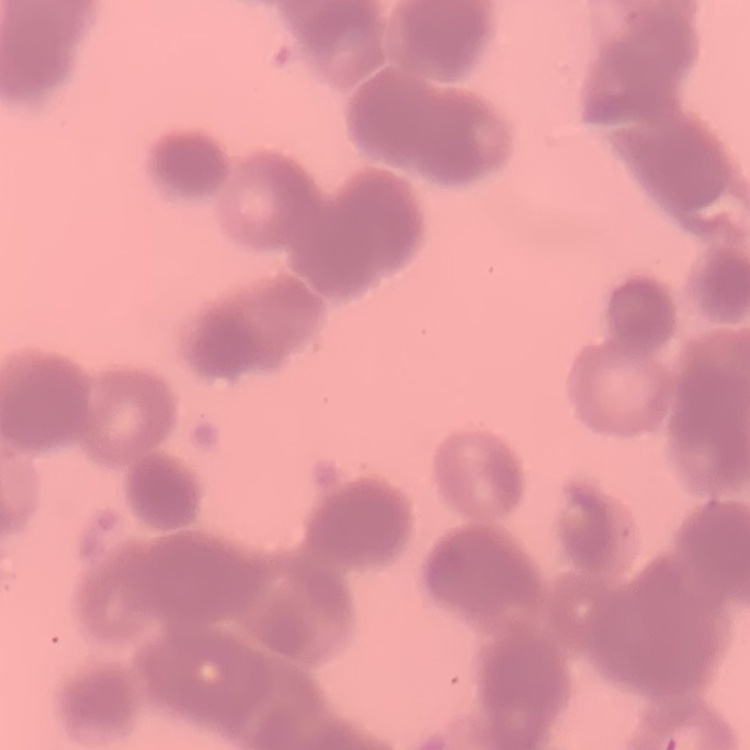
Summary:
  - Red blood cell morphology: rouleaux formation
  - Image type: square crop of a larger photomicrograph
  - Preparation: thin blood smear
  - Stain: Field's or Giemsa